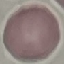
{
  "result": "no malaria parasites seen",
  "stain": "Giemsa",
  "preparation": "thin blood film",
  "image_type": "cell patch, automatically extracted from a larger field of view and resized to 64 × 64 pixels",
  "capture": "smartphone camera at the microscope eyepiece"
}